Classify this cell by malaria status.
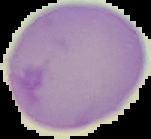

It is parasitized.

preparation: thin blood smear
image_type: segmented cell region with the area outside set to black
image_size: 151×139 pixels